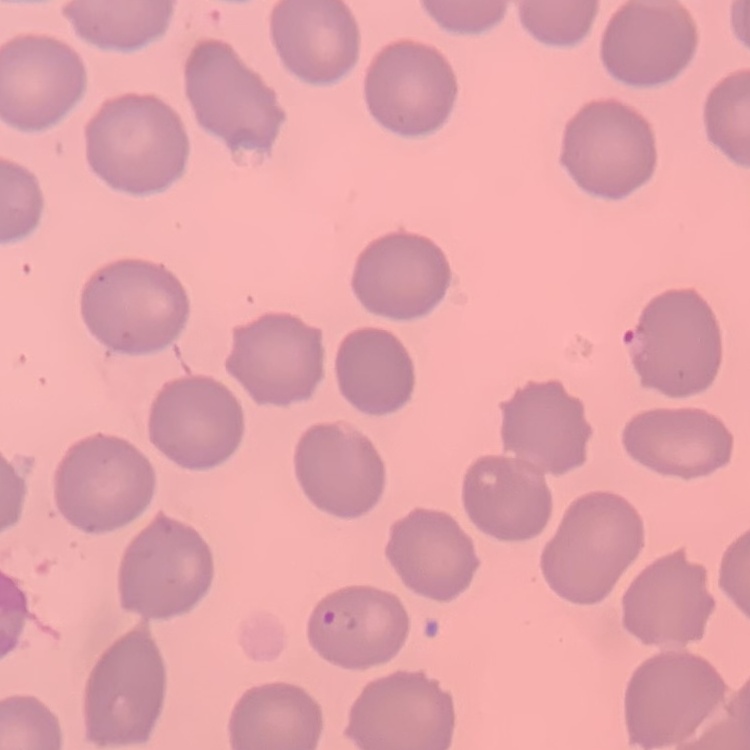

The erythrocytes exhibit no rouleaux formation. Square crop of a larger photomicrograph. Thin blood smear. Stained with either Field's or Giemsa.